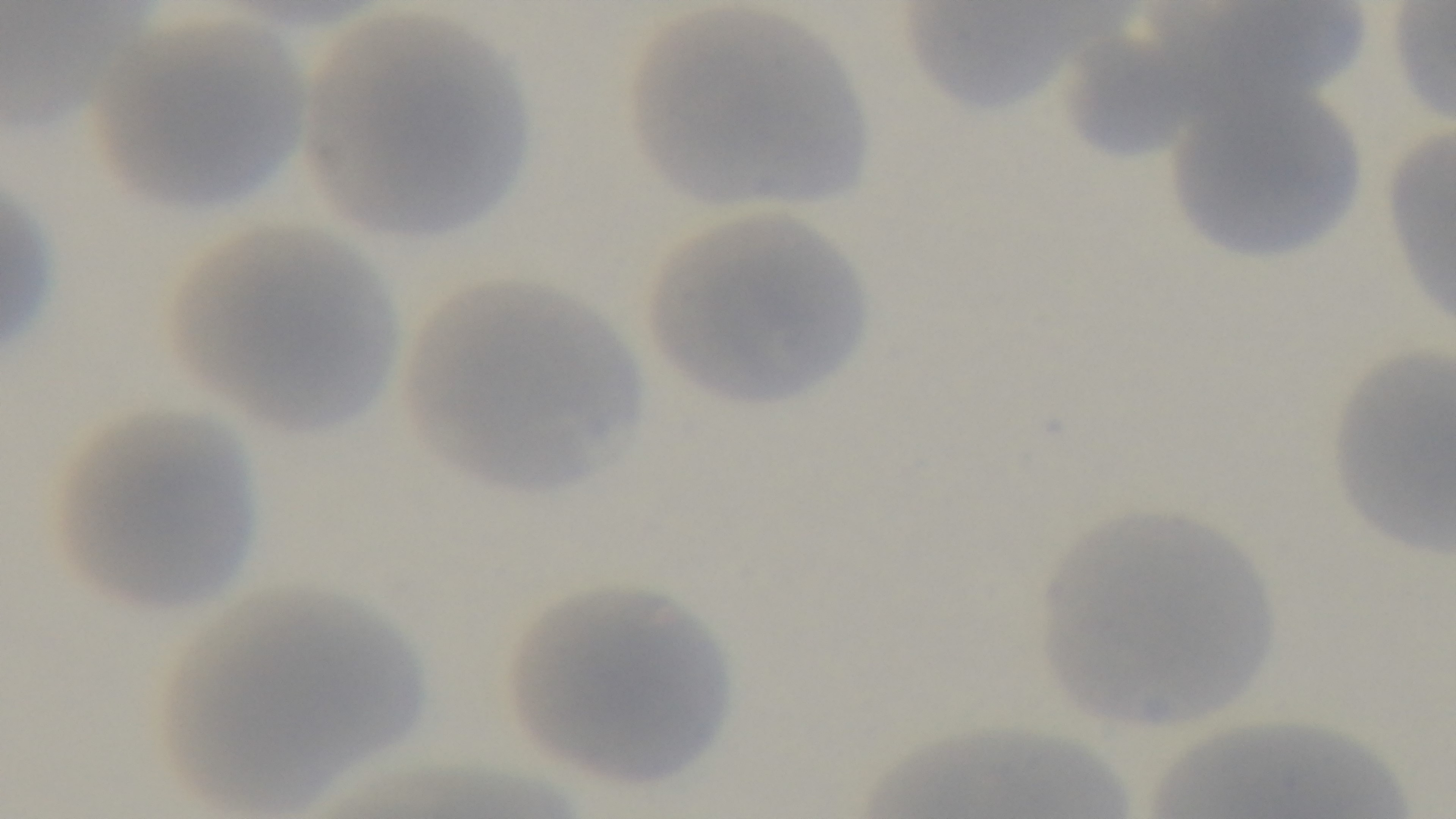
Summary:
  - Field of view: one from the slide
  - Capture: mounted 4K digital camera
  - Stain: Giemsa
  - Malaria status: negative
  - Objective: 100x oil immersion
  - Preparation: thin smear
  - Modality: light microscopy